Give the position of every Plasmodium parasite visible.
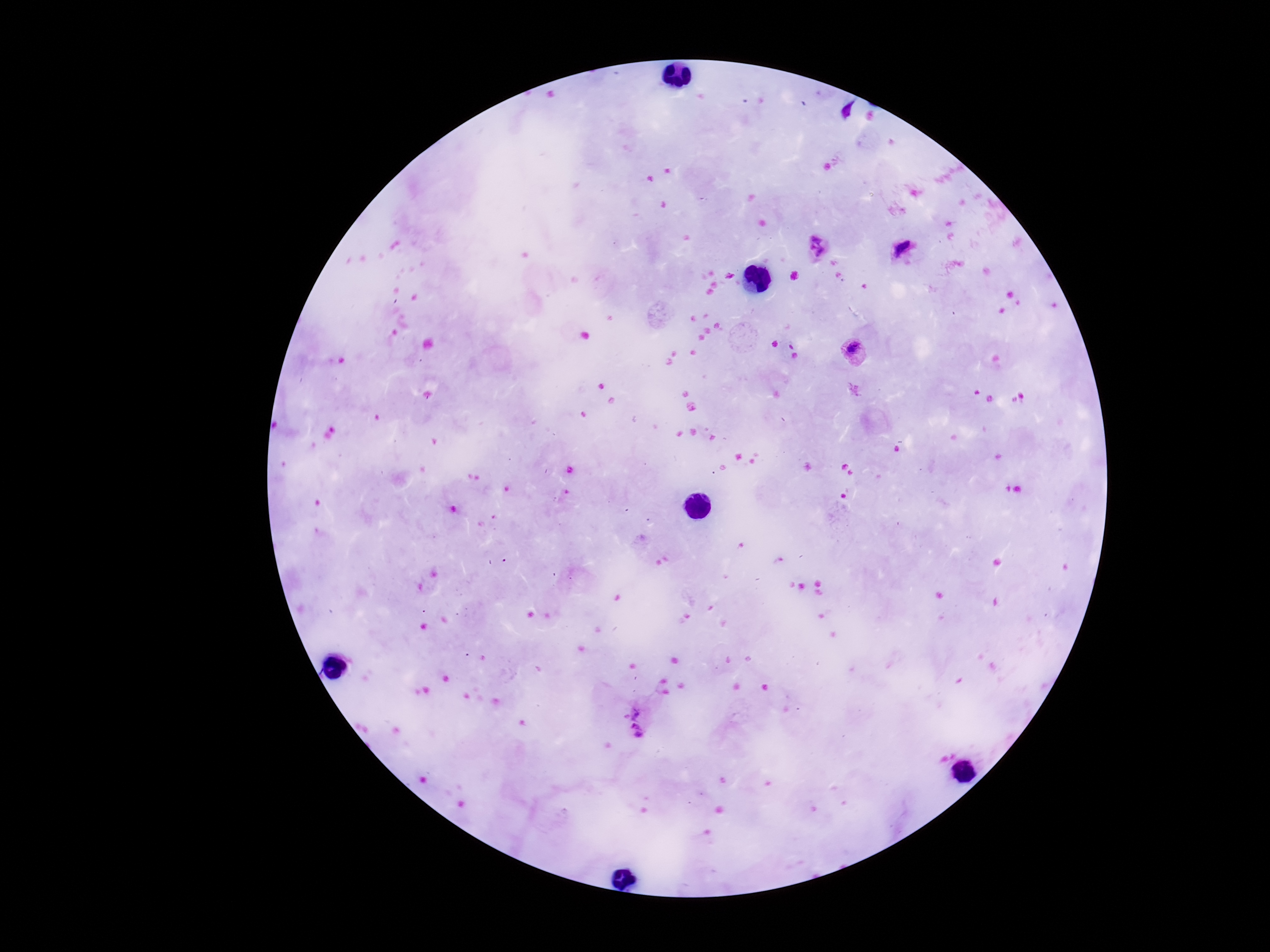

Approximate object centers, in pixels from the top-left corner.
Plasmodium parasites: (x=817, y=249), (x=907, y=252), (x=855, y=352), (x=638, y=721).

100x magnification. Smartphone photograph taken through the microscope eyepiece. Image is 1270×952 pixels. Giemsa-stained preparation. Patient malaria status: infected. One field from this slide. Thick blood smear.